Locate and identify every blood parasite.
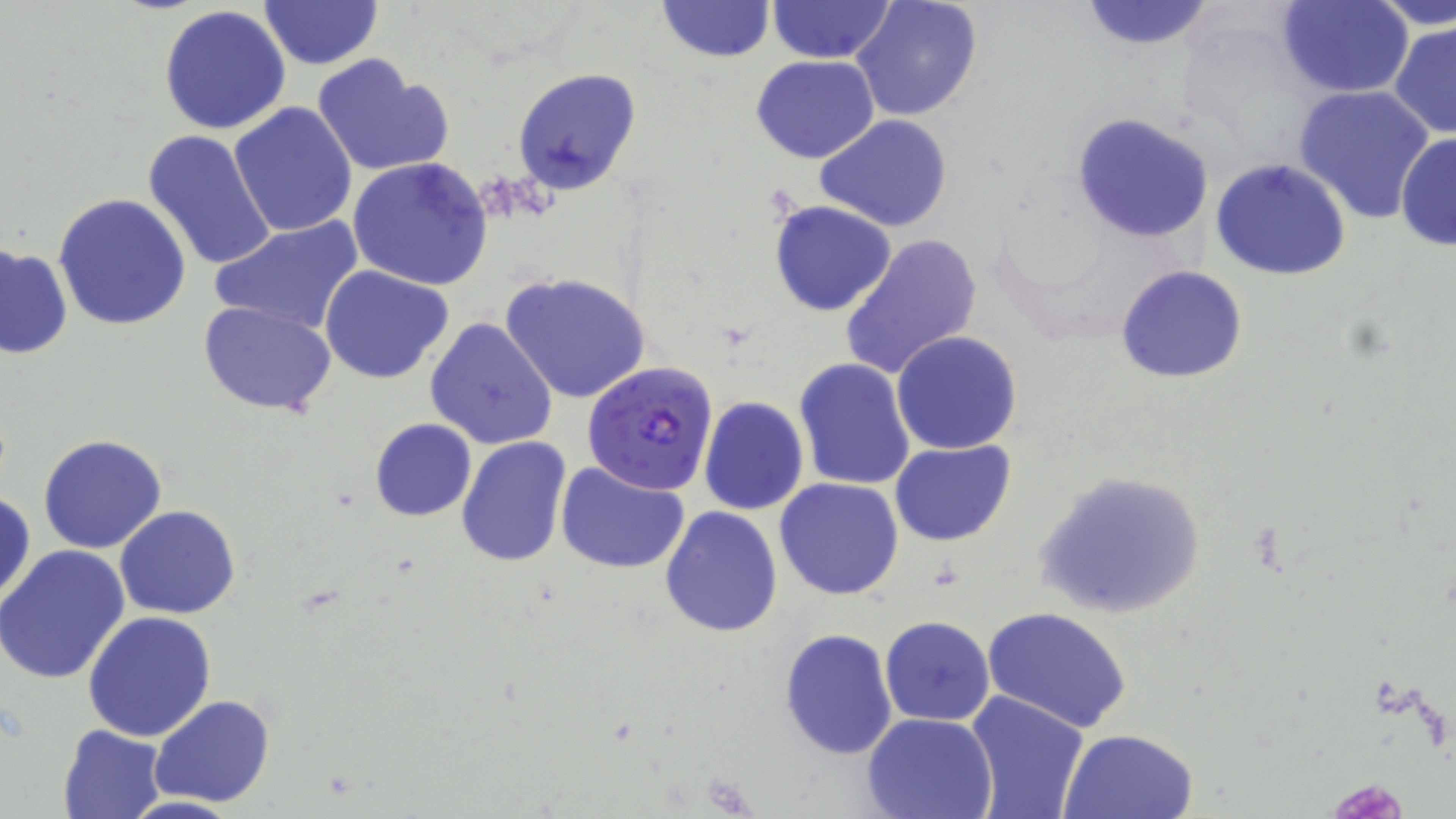
Approximate bounding boxes as named x1/y1/x2/y2 corners in pixels.
Plasmodium falciparum-infected red blood cells: (x1=582, y1=359, x2=718, y2=498).
No Plasmodium ovale, Plasmodium malariae, Plasmodium vivax, Babesia divergens, or Trypanosoma brucei observed.

Uninfected red blood cell locations: (x1=851, y1=0, x2=984, y2=121), (x1=1075, y1=0, x2=1221, y2=52), (x1=1276, y1=0, x2=1414, y2=97), (x1=1371, y1=0, x2=1456, y2=31), (x1=260, y1=1, x2=382, y2=70), (x1=656, y1=1, x2=775, y2=63), (x1=767, y1=1, x2=896, y2=65), (x1=158, y1=5, x2=293, y2=137), (x1=1390, y1=20, x2=1456, y2=141), (x1=311, y1=54, x2=453, y2=179), (x1=751, y1=54, x2=878, y2=164), (x1=512, y1=66, x2=641, y2=194), (x1=1293, y1=84, x2=1437, y2=223), (x1=229, y1=102, x2=359, y2=238), (x1=1072, y1=112, x2=1213, y2=244), (x1=815, y1=115, x2=954, y2=233), (x1=142, y1=128, x2=278, y2=270), (x1=1395, y1=130, x2=1456, y2=252), (x1=347, y1=157, x2=493, y2=290), (x1=1210, y1=158, x2=1351, y2=281), (x1=52, y1=192, x2=192, y2=331), (x1=767, y1=200, x2=898, y2=318), (x1=211, y1=216, x2=365, y2=336), (x1=839, y1=233, x2=984, y2=383), (x1=1, y1=243, x2=72, y2=360), (x1=321, y1=265, x2=456, y2=383), (x1=1116, y1=265, x2=1248, y2=384), (x1=499, y1=272, x2=653, y2=407), (x1=199, y1=302, x2=335, y2=417), (x1=425, y1=316, x2=557, y2=450), (x1=891, y1=331, x2=1023, y2=455), (x1=794, y1=357, x2=916, y2=491), (x1=699, y1=396, x2=808, y2=514), (x1=369, y1=418, x2=477, y2=521), (x1=38, y1=434, x2=168, y2=555), (x1=456, y1=436, x2=573, y2=570), (x1=889, y1=439, x2=1017, y2=546), (x1=556, y1=460, x2=690, y2=573), (x1=1032, y1=469, x2=1207, y2=620), (x1=775, y1=477, x2=904, y2=599), (x1=1, y1=488, x2=36, y2=609), (x1=116, y1=504, x2=239, y2=619), (x1=660, y1=506, x2=783, y2=635), (x1=0, y1=546, x2=132, y2=684), (x1=981, y1=605, x2=1132, y2=734), (x1=83, y1=610, x2=216, y2=742), (x1=879, y1=615, x2=996, y2=726), (x1=779, y1=627, x2=898, y2=761), (x1=965, y1=691, x2=1090, y2=819), (x1=150, y1=695, x2=275, y2=806), (x1=864, y1=713, x2=997, y2=819), (x1=58, y1=724, x2=168, y2=819), (x1=1060, y1=728, x2=1198, y2=819). Slide-level diagnosis: Plasmodium falciparum. Single field of view. Image is 1456×819 pixels. Optical microscopy. Thin blood smear. Captured at 1000x magnification. May-Grünwald-Giemsa stain.